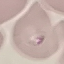

Malaria status: uninfected. Giemsa-stained preparation. Automatically extracted cell patch, resized to 64 × 64 pixels. Photographed with a smartphone camera at the microscope eyepiece. Thin blood smear.